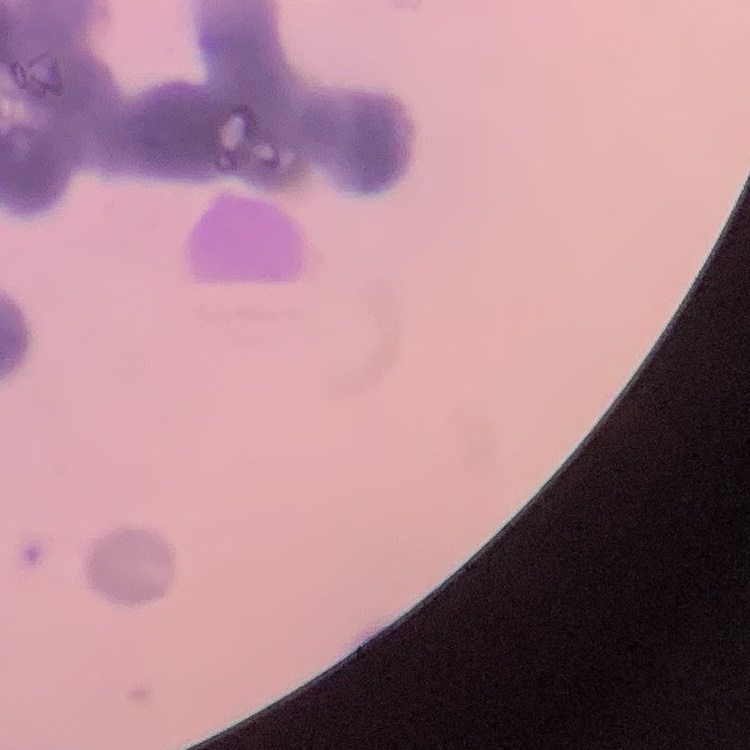

The erythrocytes show rouleaux formation. Thin blood film. Field's or Giemsa stain. Square crop of a larger photomicrograph.